Assess this cell for malaria.
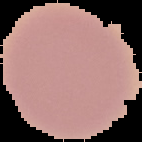

Uninfected.

Summary:
  - Image size: 142×142 pixels
  - Image type: cell region segmented out of the field of view; surrounding area masked to black
  - Preparation: thin blood film